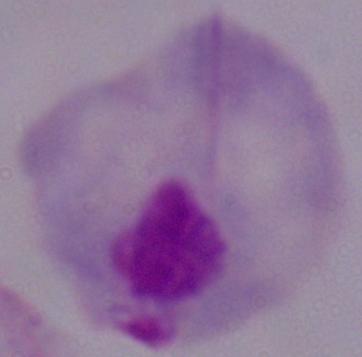
A trichomonad is seen. Micrograph. Captured at 1000x magnification.